Assess the morphology of the erythrocytes.
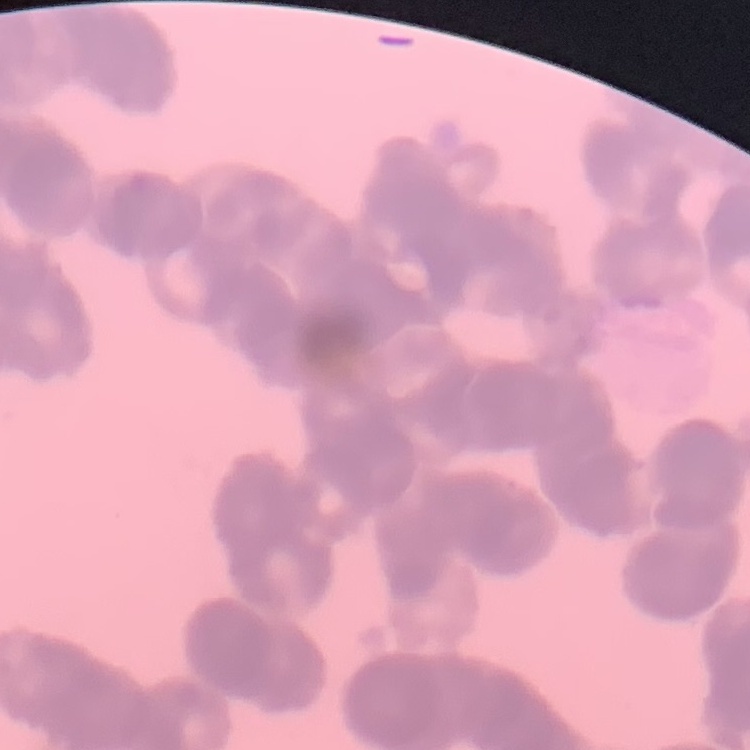
Rouleaux formation.

Summary:
  - Stain: Field's or Giemsa
  - Preparation: thin blood smear
  - Image type: one tile cut from a larger photomicrograph